Outline each uninfected red blood cell.
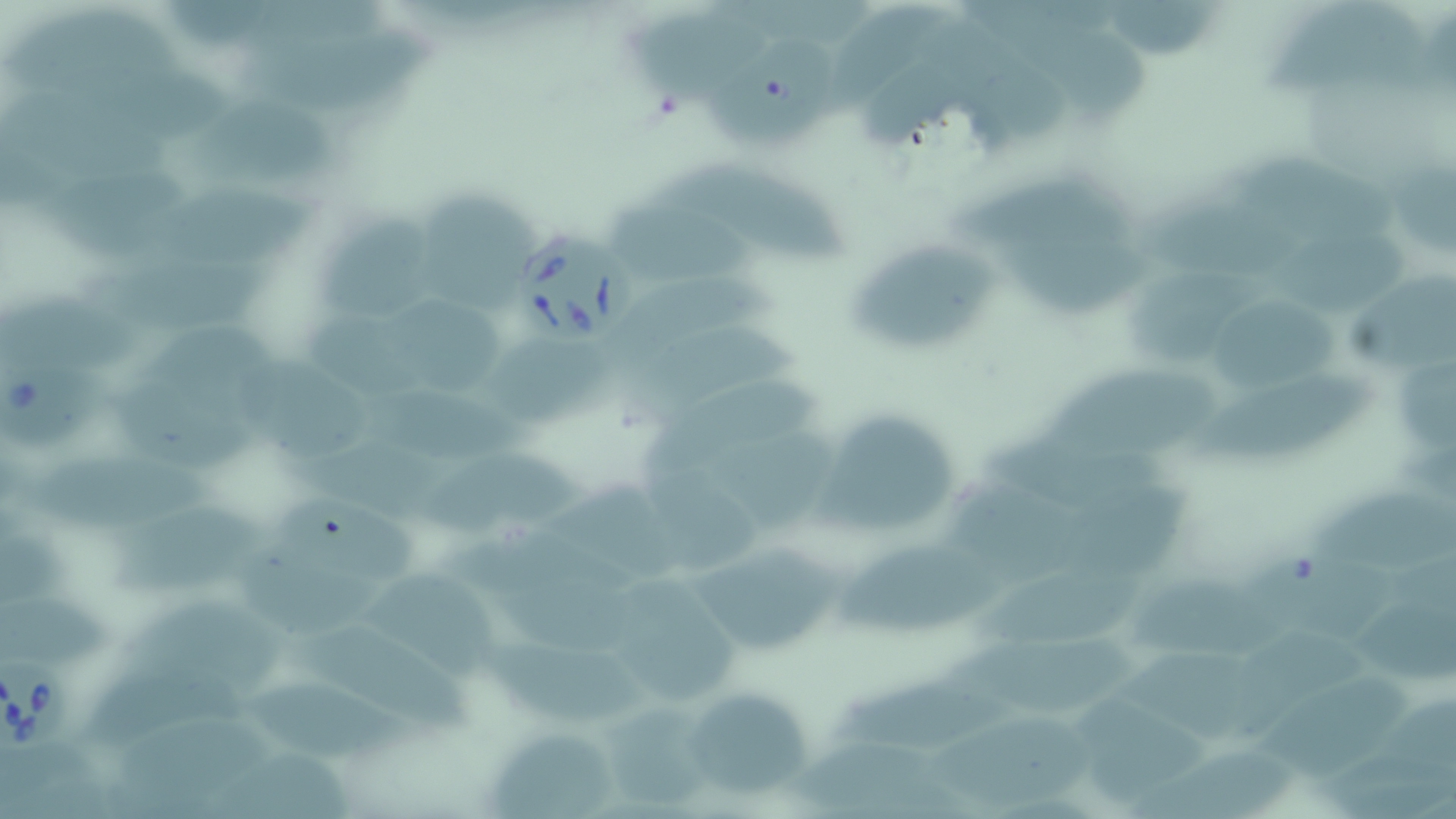

Approximate bounding boxes as [x1, y1, x2, y2] in pixels.
Uninfected red blood cells: [170, 0, 292, 50], [705, 2, 883, 48], [1256, 2, 1436, 107], [815, 6, 944, 115], [1123, 6, 1225, 57], [12, 10, 174, 81], [623, 14, 770, 104], [926, 18, 1066, 144], [706, 29, 842, 151], [1039, 29, 1152, 121], [248, 31, 446, 120], [82, 65, 232, 139], [869, 74, 971, 156], [12, 85, 170, 180], [204, 97, 334, 184], [44, 155, 189, 247], [1388, 156, 1455, 243], [661, 159, 863, 265], [1249, 161, 1400, 242], [953, 172, 1148, 253], [413, 184, 534, 312], [150, 190, 318, 270], [1149, 190, 1299, 274], [615, 200, 775, 278], [319, 215, 429, 318], [1282, 230, 1412, 326], [863, 242, 1008, 347], [1012, 242, 1148, 314], [86, 253, 276, 330], [1353, 261, 1456, 367], [1129, 267, 1272, 373], [615, 270, 787, 361], [5, 286, 145, 376], [1213, 288, 1349, 389], [401, 294, 505, 388], [312, 313, 421, 414], [147, 316, 277, 391], [618, 321, 799, 416], [489, 345, 615, 424], [243, 348, 379, 469], [1386, 349, 1455, 434], [1062, 361, 1221, 446], [1197, 368, 1382, 452], [113, 376, 260, 479], [645, 380, 824, 470], [359, 388, 564, 466], [824, 415, 956, 526], [987, 417, 1168, 506], [725, 428, 841, 522], [308, 434, 501, 518], [37, 446, 222, 536], [434, 447, 582, 529], [643, 462, 767, 568], [551, 479, 676, 573], [1064, 481, 1200, 569], [1317, 485, 1456, 568], [957, 490, 1090, 570], [275, 497, 426, 585], [125, 513, 276, 596], [448, 523, 646, 597], [4, 537, 84, 608], [839, 541, 1020, 628], [693, 547, 845, 651], [1248, 552, 1385, 625], [241, 558, 385, 635], [980, 560, 1161, 635], [382, 565, 503, 678], [499, 569, 654, 659], [1136, 577, 1274, 647], [625, 588, 737, 706], [4, 597, 109, 667], [130, 598, 291, 692], [1354, 601, 1452, 676], [957, 623, 1146, 703], [1213, 627, 1362, 729], [303, 635, 477, 737], [503, 640, 658, 730], [1123, 643, 1239, 726], [843, 660, 1024, 742], [1258, 668, 1413, 759], [80, 669, 259, 750], [264, 682, 414, 763], [686, 691, 812, 798], [1339, 691, 1456, 817], [1082, 698, 1213, 804], [610, 703, 723, 802], [933, 707, 1094, 802], [125, 715, 283, 793], [495, 723, 610, 819], [799, 729, 932, 808], [4, 737, 105, 819], [1133, 742, 1295, 817], [220, 758, 351, 819].

slide_level_diagnosis: Babesia divergens
stain: May-Grünwald-Giemsa
babesia_divergens_infected_red_blood_cell_locations: 'approximate bounding boxes as [x1, y1, x2, y2] in pixels: [520, 232, 638, 344], [1, 357, 117, 446], [1, 654, 71, 757]'
image_size: 1456×819 pixels
preparation: thin blood film
modality: optical microscopy
field_of_view: single
magnification: 1000x